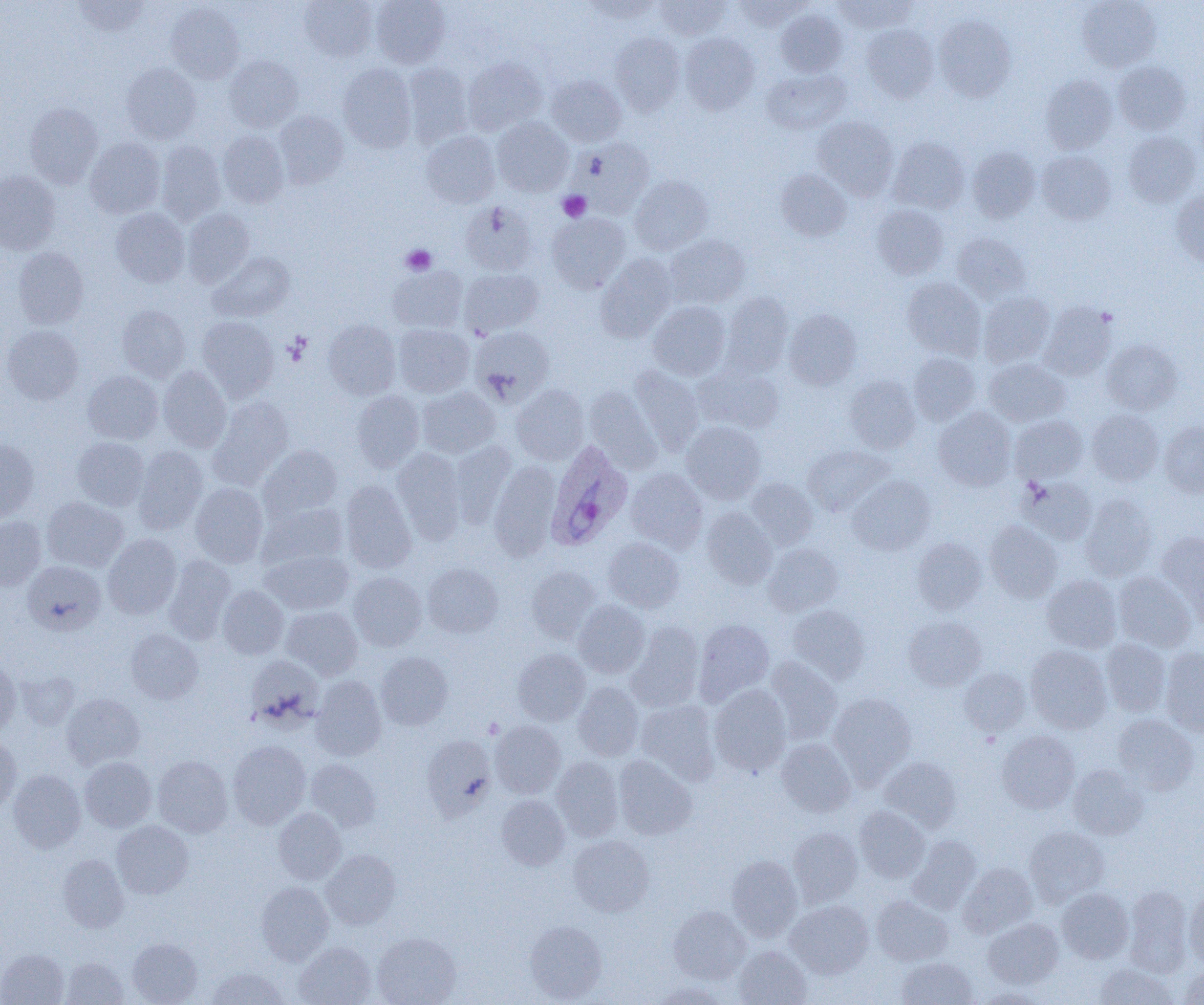

slide-level diagnosis = Plasmodium ovale
image size = 1204×1005 pixels
platelet locations = approximate bounding boxes as (x1,y1)-(x2,y2) corner pairs in pixels: (558,191)-(591,222), (401,244)-(437,275)
uninfected red blood cell locations = approximate bounding boxes as (x1,y1)-(x2,y2) corner pairs in pixels: (73,0)-(149,36), (299,0)-(378,62), (371,0)-(450,68), (583,0)-(662,23), (655,0)-(731,39), (730,0)-(809,31), (833,0)-(917,32), (1076,0)-(1161,71), (166,2)-(244,84), (776,9)-(847,77), (934,15)-(1016,101), (861,25)-(939,102), (610,33)-(684,115), (680,33)-(760,114), (224,55)-(303,132), (463,58)-(547,134), (1113,61)-(1191,135), (121,62)-(201,143), (338,63)-(416,152), (403,63)-(473,147), (762,68)-(851,135), (547,75)-(627,146), (1041,75)-(1118,154), (24,102)-(103,188), (274,111)-(349,187), (812,116)-(898,200), (492,117)-(573,196), (218,130)-(289,208), (421,131)-(499,208), (1123,131)-(1201,207), (85,137)-(165,218), (889,137)-(970,214), (571,138)-(654,218), (156,141)-(226,224), (967,146)-(1040,222), (1037,150)-(1116,224), (776,169)-(851,241), (0,170)-(60,254), (629,175)-(713,254), (1171,190)-(1204,267), (460,201)-(537,275), (871,204)-(949,279), (111,208)-(190,287), (182,209)-(255,287), (546,213)-(630,293), (951,233)-(1031,303), (665,234)-(750,308), (13,247)-(88,329), (209,252)-(295,321), (596,254)-(677,341), (387,266)-(468,333), (460,267)-(544,336), (902,277)-(985,359), (979,291)-(1056,368), (720,292)-(793,377), (648,302)-(731,380), (1039,302)-(1116,380), (117,305)-(190,381), (783,308)-(862,389), (197,317)-(279,400), (323,321)-(402,399), (394,324)-(474,397), (2,325)-(84,404), (470,326)-(554,404), (1102,339)-(1182,415), (908,352)-(980,425), (983,358)-(1070,426), (693,364)-(784,434), (629,365)-(705,455), (158,366)-(232,452), (83,370)-(163,444), (844,374)-(921,453), (511,384)-(589,465), (417,386)-(500,458), (585,387)-(662,473), (352,390)-(425,472), (208,396)-(294,488), (934,406)-(1017,490), (1087,410)-(1163,485), (1010,415)-(1088,483), (681,421)-(766,503), (1159,421)-(1204,497), (71,437)-(149,510), (0,438)-(39,522), (449,441)-(516,527), (802,444)-(893,517), (134,445)-(208,533), (259,445)-(342,520), (392,449)-(466,543), (489,461)-(561,560), (625,468)-(708,551), (847,475)-(935,555), (1020,477)-(1097,545), (745,478)-(818,549), (340,481)-(417,574), (190,483)-(268,567), (1080,494)-(1157,581), (42,497)-(128,571), (258,502)-(349,570), (701,508)-(778,589), (0,516)-(47,590), (985,522)-(1063,603), (1157,532)-(1204,617), (103,534)-(182,619), (912,537)-(988,615), (604,538)-(684,612), (763,543)-(843,616), (261,549)-(354,615), (163,556)-(236,644), (23,561)-(106,635), (422,562)-(503,637), (526,565)-(601,642), (349,572)-(427,651), (1113,572)-(1196,652), (1041,575)-(1123,653), (218,585)-(289,659), (573,601)-(650,678), (787,605)-(870,684), (281,606)-(363,679), (904,616)-(986,690), (694,619)-(774,704), (626,621)-(704,712), (125,629)-(203,704), (1101,639)-(1171,716), (1025,645)-(1112,733), (513,648)-(590,725), (1159,648)-(1204,737), (376,651)-(453,730), (246,655)-(324,731), (0,657)-(21,736), (764,657)-(842,744), (959,667)-(1031,735), (16,670)-(79,730), (311,675)-(386,760), (573,682)-(643,760), (709,685)-(792,776), (829,692)-(916,784), (61,693)-(145,770), (635,700)-(720,783), (1112,714)-(1199,795), (490,720)-(566,798), (997,730)-(1080,813), (421,734)-(497,818), (0,735)-(22,814), (776,738)-(856,816), (228,740)-(311,828), (152,755)-(233,837), (614,755)-(697,840), (79,756)-(156,832), (551,756)-(623,841), (879,757)-(962,831), (306,759)-(381,833), (1068,765)-(1148,839), (8,769)-(86,853), (496,795)-(570,870), (854,806)-(929,881), (273,808)-(346,884), (111,820)-(193,899), (789,827)-(862,906), (1024,827)-(1109,906), (568,835)-(654,916), (907,836)-(981,914), (320,850)-(401,929), (57,854)-(129,932), (726,855)-(802,940), (958,863)-(1037,937), (256,881)-(334,965), (1124,886)-(1193,975), (1056,888)-(1133,963), (1184,890)-(1204,968), (872,895)-(952,966), (785,900)-(873,978), (668,906)-(750,984), (983,918)-(1063,988), (524,920)-(607,1003), (372,932)-(460,1005), (127,938)-(202,1005), (294,941)-(376,1005), (734,945)-(811,1005), (0,949)-(69,1005), (60,957)-(129,1005), (896,957)-(978,1004), (1093,963)-(1177,1005), (205,966)-(288,1004), (1179,966)-(1204,1004), (650,981)-(729,1004), (976,987)-(1050,1005)
Plasmodium ovale-infected red blood cell locations = approximate bounding boxes as (x1,y1)-(x2,y2) corner pairs in pixels: (546,440)-(634,550)
magnification = 1000x
field of view = one of a larger specimen
modality = light microscopy
preparation = thin blood smear